Classify this cell by malaria status.
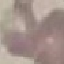

It is uninfected.

Photographed with a smartphone camera at the microscope eyepiece. Cell patch, automatically extracted from a larger field of view and resized to 64 × 64 pixels. Giemsa stain. Thin blood film.